Identify the parasite.
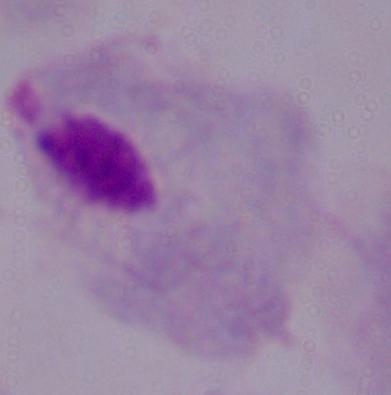

This is a trichomonad.

{
  "modality": "photomicrograph",
  "magnification": "1000x"
}